Identify the blood parasite species.
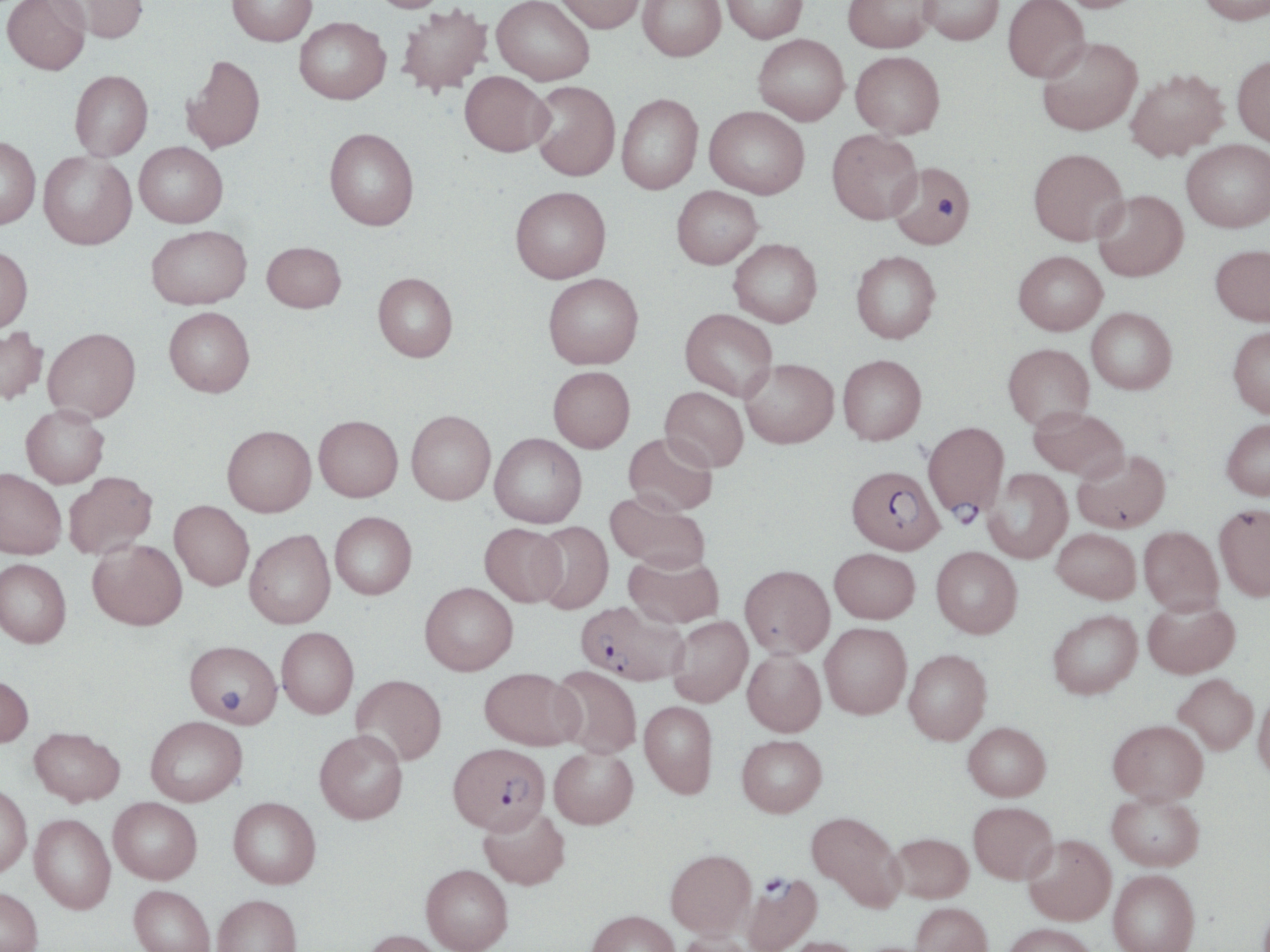

Plasmodium falciparum.

{
  "preparation": "thin blood smear",
  "field_of_view": "one of a larger specimen",
  "uninfected_red_blood_cell_locations": "approximate bounding boxes as (x1, y1, x2, y2) in pixels: (2, 0, 90, 75), (49, 0, 149, 43), (227, 0, 317, 46), (368, 0, 451, 12), (491, 0, 594, 85), (554, 0, 645, 33), (637, 0, 726, 61), (721, 0, 807, 43), (843, 0, 935, 52), (919, 0, 1004, 45), (1003, 0, 1090, 83), (1053, 0, 1147, 12), (1197, 0, 1270, 25), (396, 5, 492, 96), (294, 17, 390, 104), (753, 34, 849, 125), (1036, 37, 1143, 136), (850, 51, 945, 139), (182, 54, 265, 154), (1232, 54, 1270, 146), (1124, 68, 1229, 162), (70, 70, 153, 160), (460, 71, 553, 156), (529, 81, 620, 181), (616, 93, 702, 194), (704, 106, 809, 199), (324, 127, 419, 230), (827, 129, 923, 224), (0, 136, 41, 229), (1182, 140, 1270, 232), (135, 141, 228, 228), (1029, 148, 1128, 245), (39, 152, 137, 250), (888, 162, 976, 249), (671, 185, 763, 269), (510, 186, 611, 283), (1092, 190, 1188, 281), (146, 225, 251, 309), (728, 238, 822, 327), (262, 241, 346, 312), (1211, 244, 1270, 326), (0, 245, 33, 332), (851, 251, 941, 343), (1014, 251, 1107, 335), (373, 272, 458, 362), (543, 273, 643, 369), (164, 307, 255, 397), (1087, 307, 1176, 394), (680, 309, 778, 401), (0, 326, 48, 405), (1228, 326, 1270, 418), (43, 327, 141, 423), (1003, 343, 1094, 430), (838, 354, 926, 445), (740, 358, 839, 448), (548, 366, 635, 452), (660, 386, 749, 472), (21, 405, 109, 488), (1028, 407, 1128, 480), (407, 410, 496, 504), (314, 415, 403, 501), (1221, 418, 1270, 500), (222, 425, 316, 516), (623, 432, 717, 515), (489, 433, 586, 528), (1073, 449, 1170, 533), (0, 468, 66, 559), (982, 468, 1072, 563), (63, 471, 158, 559), (606, 491, 709, 572), (170, 500, 254, 590), (1214, 505, 1270, 600), (329, 511, 417, 599), (531, 521, 614, 614), (480, 523, 567, 606), (1139, 526, 1223, 614), (1051, 528, 1141, 604), (244, 529, 335, 628), (88, 539, 187, 630), (931, 546, 1022, 638), (830, 548, 920, 623), (624, 552, 723, 628), (0, 558, 71, 647), (740, 564, 834, 658), (420, 582, 518, 675), (1143, 598, 1239, 678), (1049, 610, 1143, 699), (667, 616, 752, 706), (820, 622, 912, 719), (277, 627, 359, 718), (186, 640, 283, 726), (904, 649, 992, 745), (742, 650, 826, 736), (550, 665, 642, 758), (480, 667, 583, 750), (1173, 673, 1258, 755), (0, 674, 33, 747), (352, 674, 447, 765), (1253, 691, 1270, 781), (639, 701, 717, 798), (145, 716, 247, 806), (1108, 719, 1208, 804), (963, 722, 1051, 801), (29, 727, 125, 806), (314, 729, 408, 824), (737, 735, 827, 816), (549, 747, 638, 829), (0, 784, 32, 878), (1107, 792, 1204, 871), (228, 796, 321, 888), (109, 797, 202, 883), (968, 801, 1057, 884), (478, 806, 570, 890), (807, 811, 905, 910), (30, 814, 116, 914), (889, 832, 973, 903), (1023, 834, 1116, 925), (666, 849, 756, 938), (421, 864, 513, 952), (1108, 869, 1200, 952), (128, 885, 215, 952), (0, 887, 42, 952), (212, 894, 302, 952), (910, 902, 993, 952), (586, 910, 680, 952), (1002, 923, 1098, 952), (362, 929, 447, 952), (674, 931, 757, 952), (777, 937, 866, 952)",
  "modality": "optical microscopy",
  "plasmodium_falciparum_infected_red_blood_cell_locations": "approximate bounding boxes as (x1, y1, x2, y2) in pixels: (922, 420, 1009, 520), (847, 465, 944, 554), (576, 600, 688, 686), (448, 742, 550, 834), (742, 875, 822, 952)",
  "platelet_locations": "approximate bounding boxes as (x1, y1, x2, y2) in pixels: (938, 198, 957, 219), (218, 690, 243, 712)",
  "stain": "May-Grünwald-Giemsa",
  "image_size": "1270×952 pixels",
  "magnification": "1000x"
}